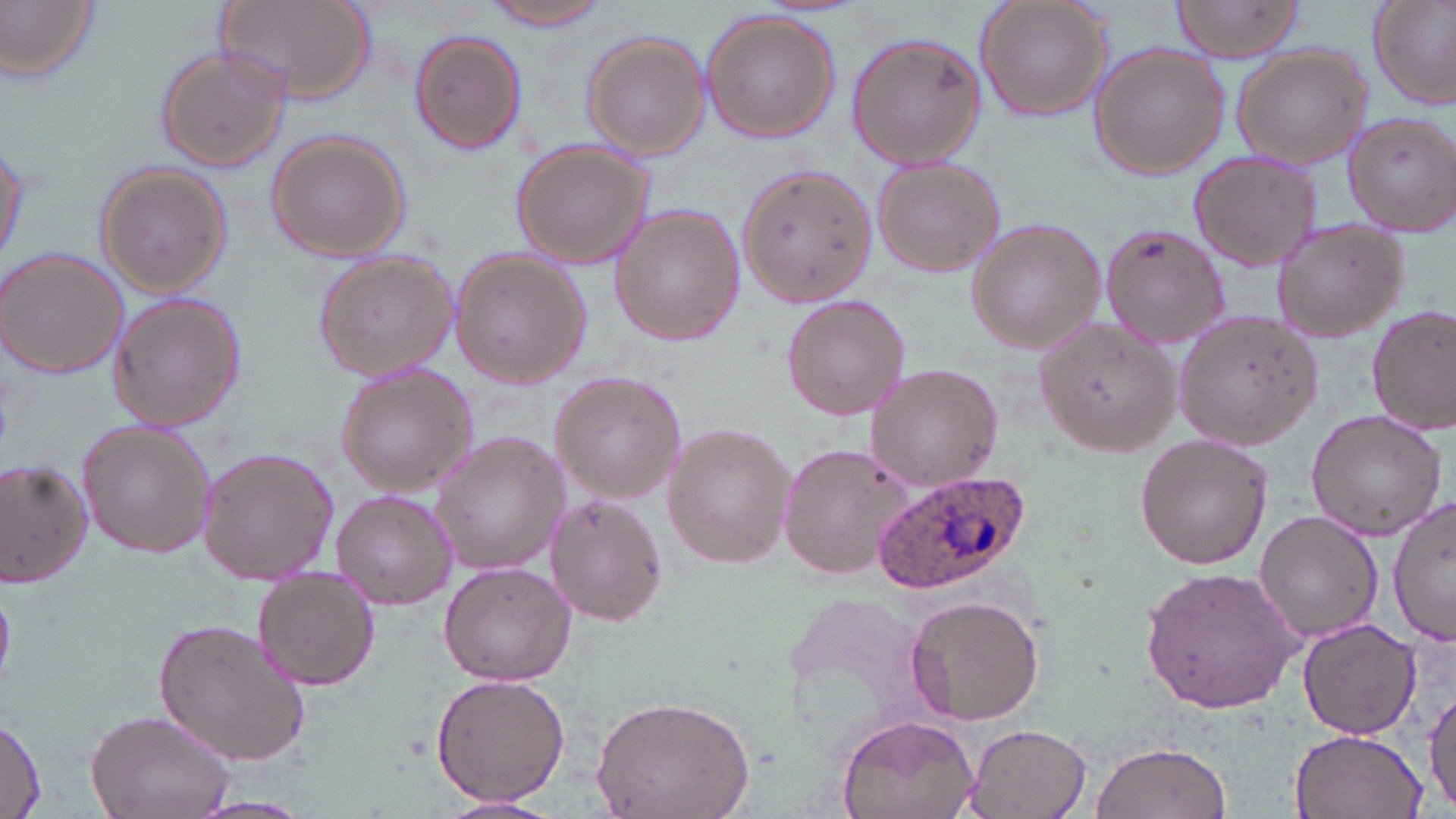 Approximate bounding boxes as (x1, y1, x2, y2) in pixels. Plasmodium ovale-infected red blood cell locations: (874, 468, 1031, 594). Uninfected red blood cell locations: (0, 0, 102, 84), (219, 0, 377, 104), (484, 0, 617, 29), (975, 0, 1114, 122), (1167, 0, 1308, 63), (1367, 2, 1456, 109), (699, 9, 842, 143), (409, 31, 526, 154), (582, 32, 706, 161), (847, 33, 987, 169), (1089, 44, 1228, 180), (1230, 45, 1373, 169), (155, 46, 291, 174), (1344, 113, 1456, 238), (266, 131, 410, 261), (1, 137, 29, 270), (510, 138, 655, 270), (1187, 149, 1322, 273), (872, 156, 1004, 276), (736, 163, 879, 308), (94, 165, 231, 300), (610, 207, 745, 344), (966, 216, 1104, 355), (1271, 220, 1411, 344), (1099, 223, 1232, 352), (1, 247, 127, 379), (451, 249, 591, 387), (314, 251, 457, 383), (107, 290, 248, 431), (783, 296, 912, 421), (1367, 305, 1456, 433), (1173, 307, 1323, 452), (1035, 316, 1180, 459), (866, 363, 1005, 491), (337, 364, 480, 497), (549, 371, 685, 503), (1306, 407, 1449, 540), (77, 420, 216, 557), (663, 422, 795, 568), (431, 434, 572, 573), (1136, 435, 1273, 569), (779, 442, 917, 582), (198, 448, 337, 586), (1, 460, 92, 589), (332, 488, 456, 608), (545, 495, 665, 627), (1388, 495, 1454, 647), (1255, 511, 1384, 645), (437, 561, 574, 686), (1141, 566, 1303, 714), (254, 567, 379, 691), (904, 592, 1047, 727), (1296, 615, 1422, 738), (154, 616, 309, 767), (431, 673, 569, 808), (1422, 682, 1455, 814), (590, 695, 755, 819), (85, 707, 235, 819), (835, 715, 980, 819), (0, 717, 45, 818), (962, 725, 1092, 818), (1288, 728, 1426, 819), (1090, 740, 1231, 819), (188, 798, 315, 818), (434, 798, 561, 819). Slide-level diagnosis: Plasmodium ovale. Image is 1456×819 pixels. Captured at 1000x magnification. Light microscopy. Thin blood smear. One field of a larger specimen. May-Grünwald-Giemsa stain.